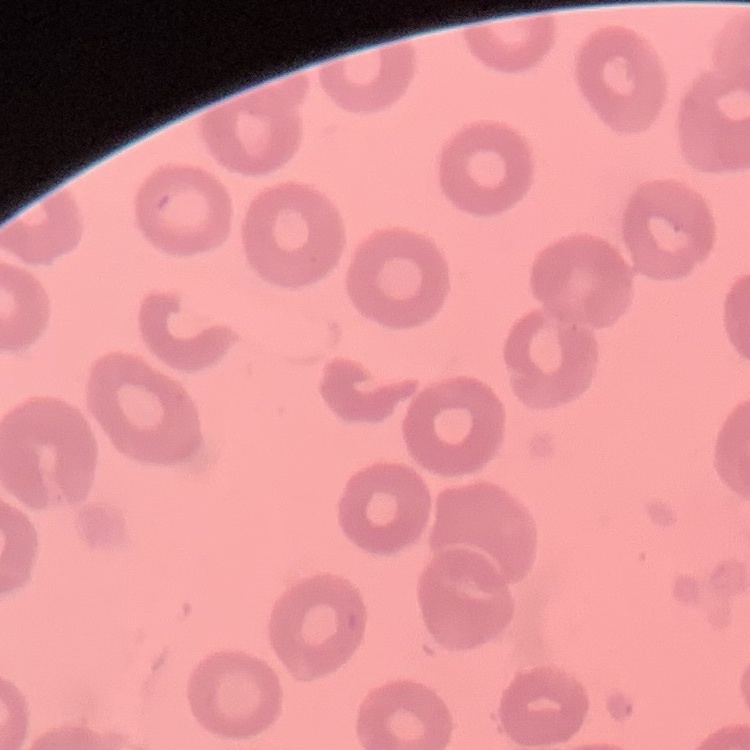
red blood cell morphology = no rouleaux formation
image type = square crop of a larger photomicrograph
stain = Field's or Giemsa
preparation = thin peripheral smear